Assess the morphology of the erythrocytes.
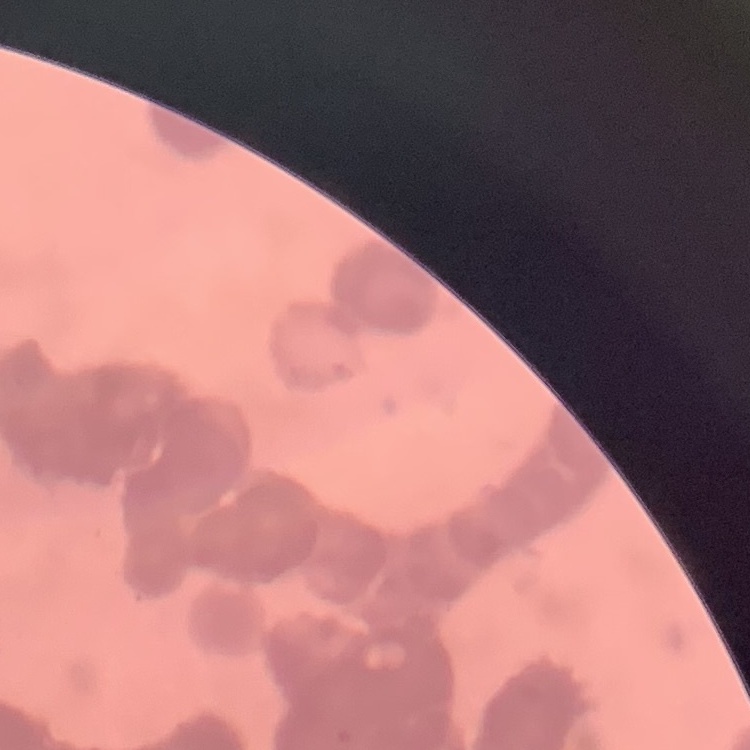
They show rouleaux formation.

image type = square crop of a larger photomicrograph
preparation = thin peripheral smear
stain = Field's or Giemsa